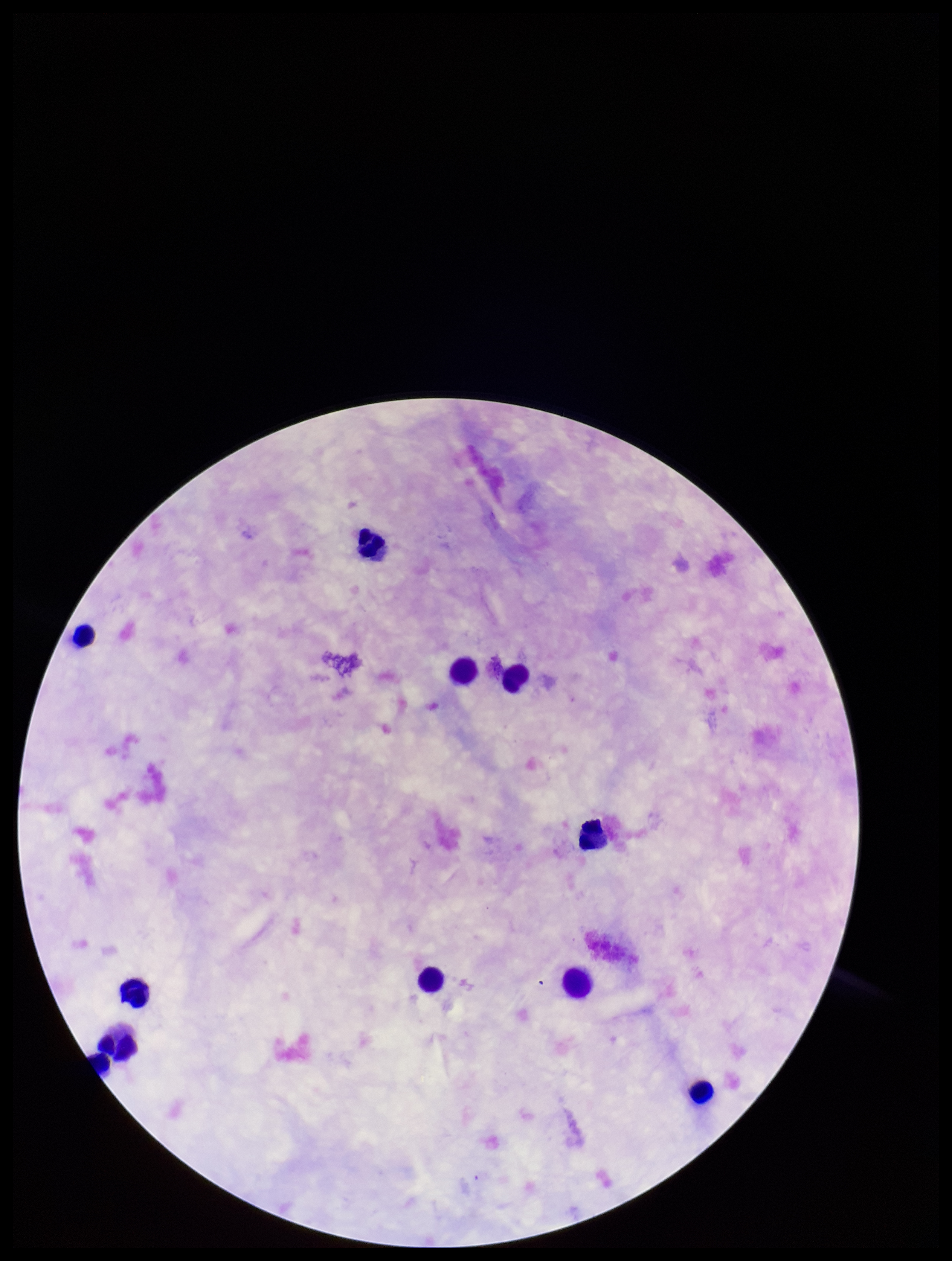

Leukocyte count: 11. Parasite count: 0. Single field of view. Plasmodium parasites: none seen. Preparation: thick smear. Photographed through the microscope eyepiece with a smartphone camera. Image is 952×1261 pixels. Patient malaria status: negative. Stained with Giemsa.